Give the extent of all Plasmodium malariae-infected red blood cells.
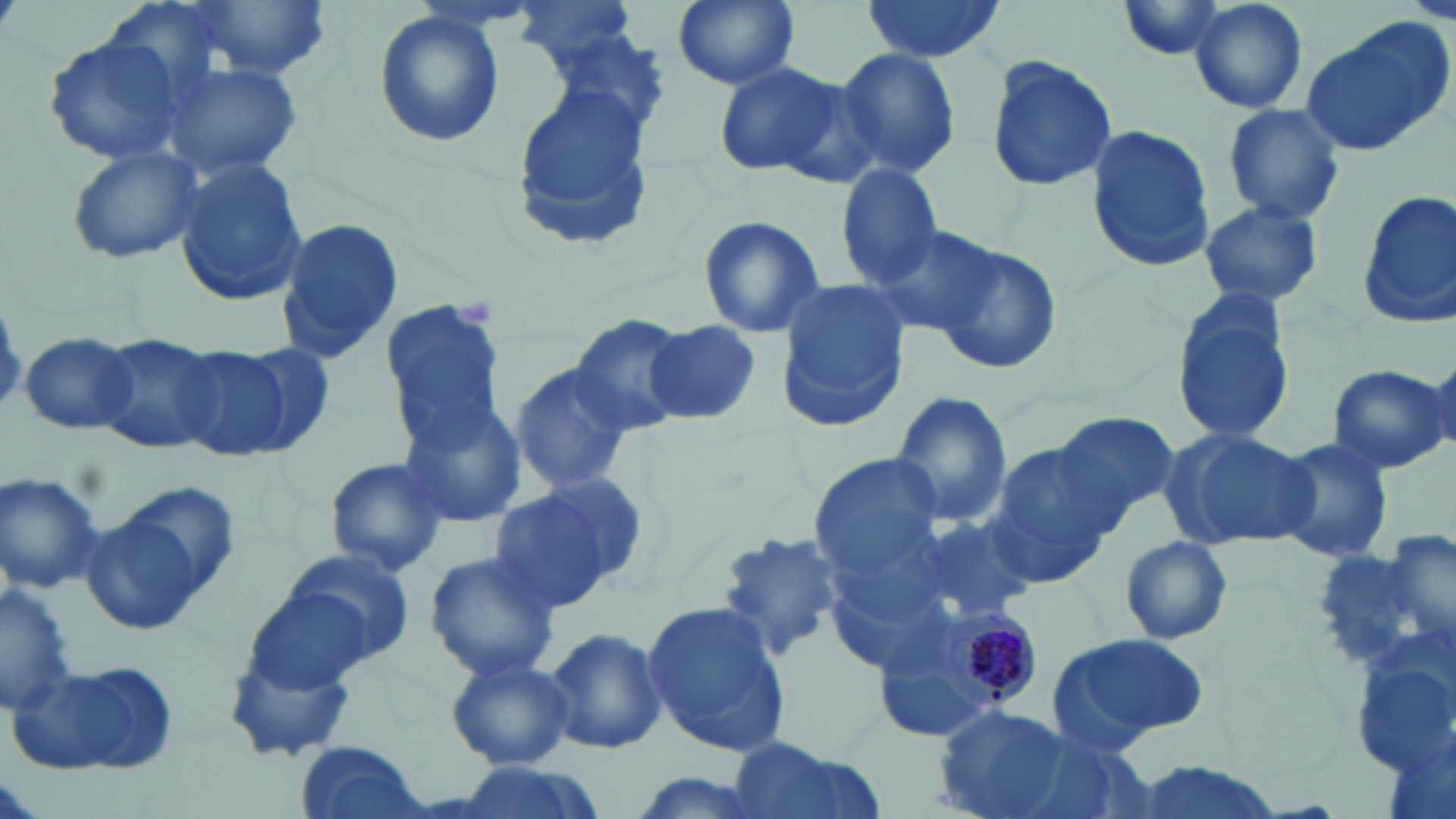

Approximate bounding boxes as (x1, y1, x2, y2) in pixels.
Plasmodium malariae-infected red blood cells: (932, 604, 1042, 712).

slide-level diagnosis = Plasmodium malariae
image size = 1456×819 pixels
uninfected red blood cell locations = approximate bounding boxes as (x1, y1, x2, y2) in pixels: (190, 0, 333, 79), (670, 0, 800, 90), (858, 0, 1007, 63), (1185, 0, 1309, 115), (511, 1, 642, 68), (1112, 2, 1236, 63), (370, 11, 506, 148), (1299, 22, 1448, 156), (541, 28, 673, 141), (43, 34, 187, 165), (834, 48, 961, 179), (983, 55, 1121, 192), (161, 59, 305, 184), (715, 61, 850, 177), (510, 80, 658, 254), (1220, 102, 1346, 225), (1086, 124, 1215, 273), (66, 141, 208, 265), (175, 154, 309, 309), (836, 163, 944, 287), (1355, 189, 1456, 329), (1198, 200, 1325, 309), (274, 215, 406, 367), (698, 215, 828, 340), (864, 218, 999, 336), (927, 239, 1064, 375), (772, 280, 911, 434), (1167, 287, 1298, 448), (377, 298, 507, 443), (565, 311, 694, 434), (644, 320, 763, 425), (20, 330, 139, 434), (95, 333, 226, 455), (235, 341, 337, 456), (167, 345, 290, 462), (1422, 348, 1456, 459), (509, 361, 635, 495), (1325, 363, 1451, 474), (891, 391, 1013, 529), (396, 397, 527, 529), (1054, 410, 1175, 536), (1160, 427, 1318, 552), (1273, 437, 1394, 566), (982, 443, 1121, 584), (809, 453, 945, 577), (324, 458, 449, 578), (0, 472, 104, 596), (488, 480, 635, 611), (80, 488, 231, 633), (913, 513, 1035, 623), (715, 527, 850, 663), (1373, 530, 1454, 662), (1117, 534, 1234, 645), (279, 546, 416, 669), (424, 552, 562, 682), (0, 582, 80, 718), (243, 585, 373, 698), (643, 600, 793, 759), (544, 626, 668, 757), (1049, 633, 1211, 752), (446, 655, 574, 770), (9, 657, 180, 779), (936, 706, 1074, 819), (722, 737, 885, 819), (295, 741, 433, 819), (1124, 759, 1288, 819), (443, 762, 613, 819), (618, 771, 776, 819)
platelet locations = approximate bounding boxes as (x1, y1, x2, y2) in pixels: (454, 298, 495, 328)
field of view = single
magnification = 1000x
stain = May-Grünwald-Giemsa
modality = optical microscopy
preparation = thin blood film